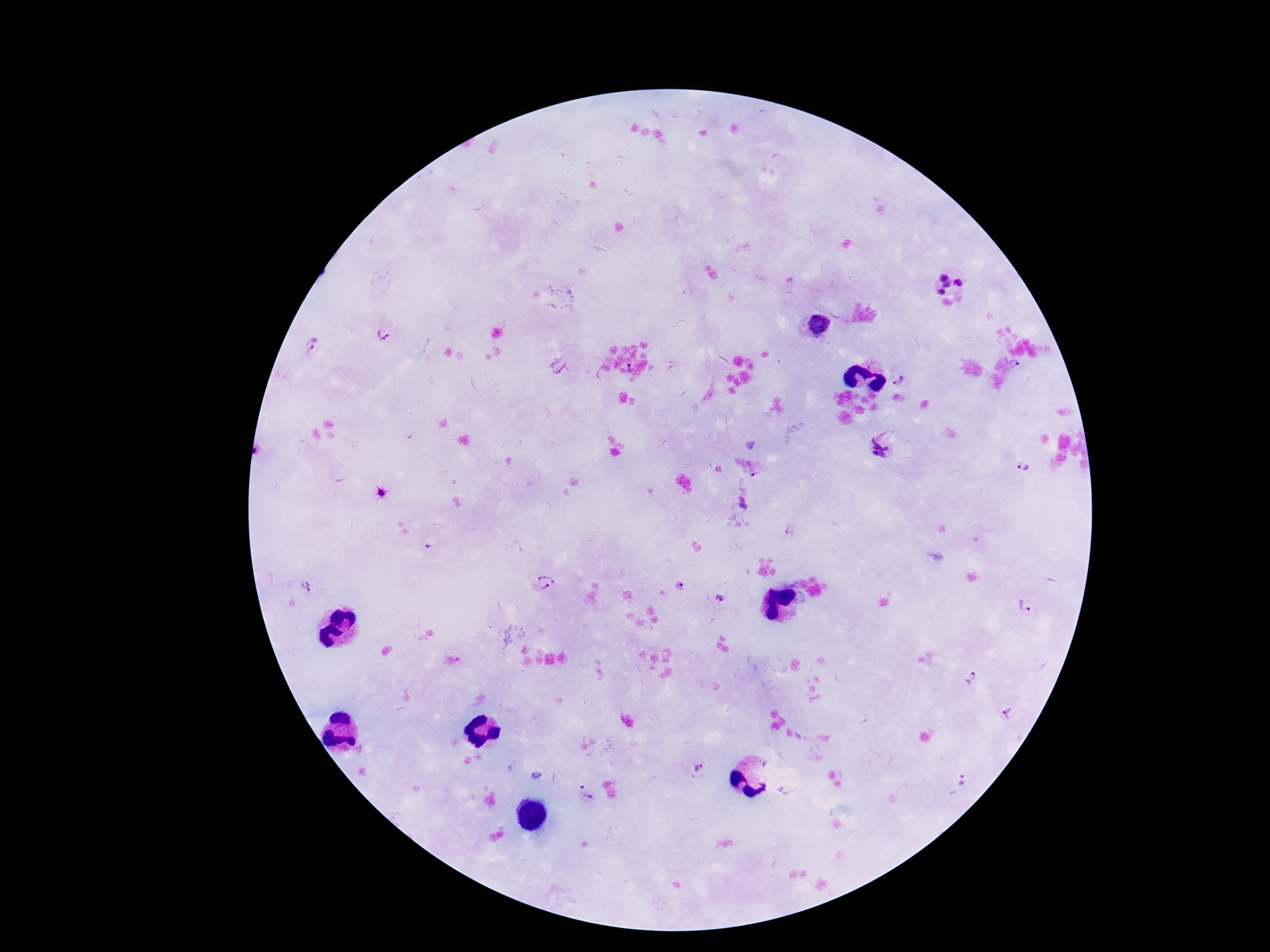
preparation = thick blood film
patient malaria status = infected
Plasmodium parasite locations = approximate centers as (x, y) in pixels: (944, 278), (958, 283), (948, 286), (941, 292), (819, 325), (382, 334), (312, 346), (1011, 361), (898, 381), (882, 447), (1025, 467), (753, 472), (428, 547), (545, 583), (305, 586), (680, 586), (720, 598), (1026, 605), (971, 678), (1008, 715), (698, 769), (961, 780), (586, 793)
field of view = one from this slide
stain = Giemsa
image size = 1270×952 pixels
capture = smartphone camera through the microscope eyepiece
magnification = 100x